Assess this cell for malaria.
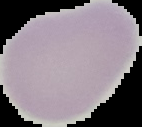

It is uninfected.

Summary:
  - Preparation: thin blood film
  - Image type: cell region segmented out of the field of view; surrounding area masked to black
  - Image size: 142×127 pixels